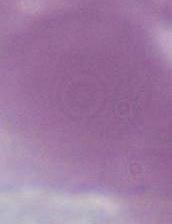

{
  "identification": "erythrocyte",
  "magnification": "1000x",
  "modality": "photomicrograph"
}